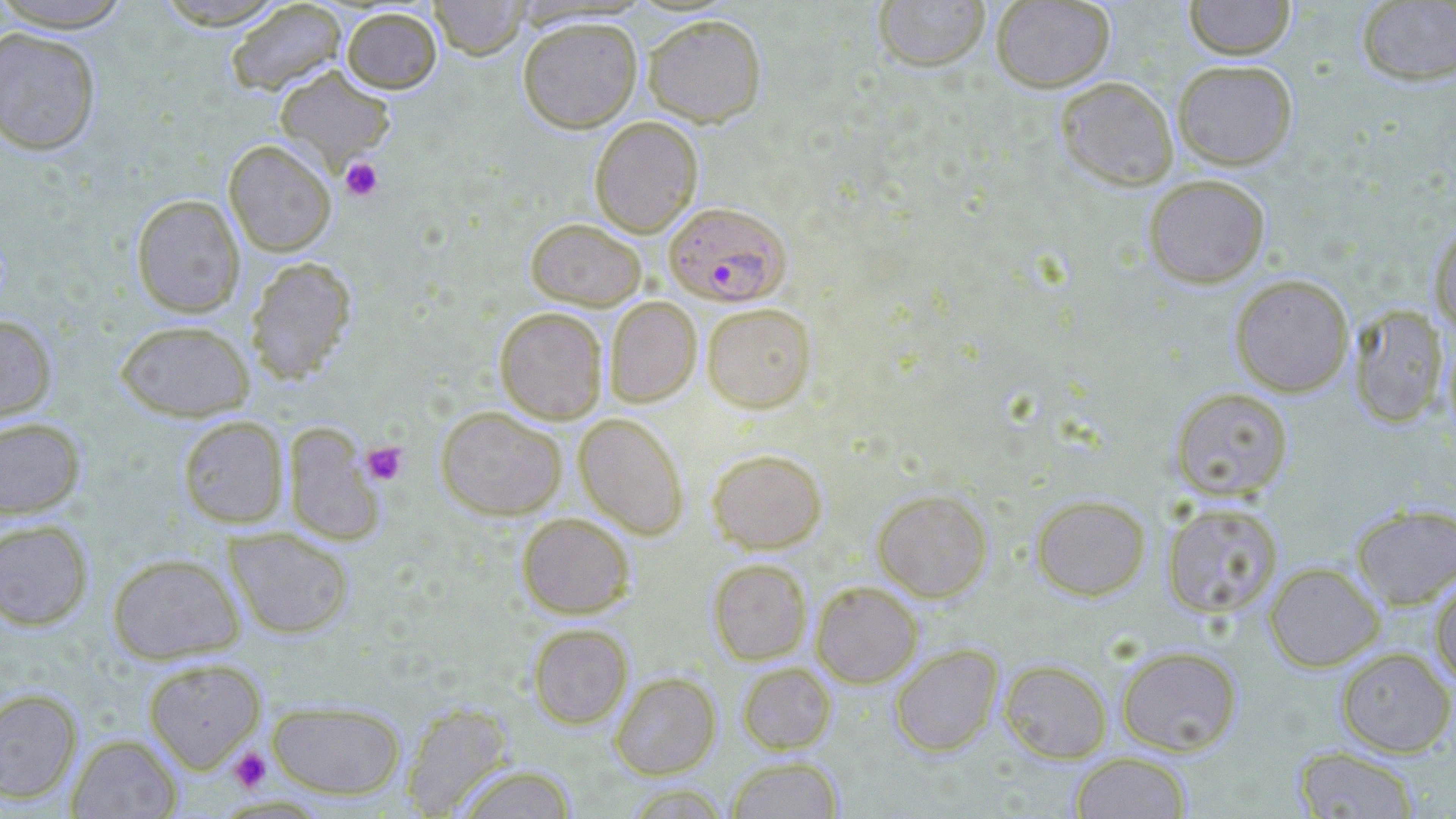

Summary:
  - Coordinate format: approximate bounding boxes as (x1,y1)-(x2,y2) corner pairs in pixels
  - Platelet locations: (340,157)-(383,201), (361,441)-(408,485), (228,747)-(272,792)
  - Uninfected red blood cell locations: (0,0)-(135,32), (150,0)-(290,29), (428,0)-(529,60), (873,0)-(990,72), (991,0)-(1114,92), (1184,0)-(1295,59), (225,1)-(347,97), (1356,1)-(1456,86), (341,6)-(442,93), (642,13)-(767,126), (517,16)-(642,133), (0,27)-(102,155), (1172,60)-(1297,169), (274,65)-(396,170), (1056,76)-(1178,190), (589,116)-(703,237), (223,139)-(337,256), (1143,174)-(1270,288), (131,194)-(245,317), (525,217)-(647,310), (1429,222)-(1456,333), (245,256)-(357,385), (1229,274)-(1354,397), (605,296)-(702,407), (702,303)-(816,412), (1348,304)-(1449,428), (494,306)-(608,424), (0,314)-(57,424), (115,319)-(255,421), (1442,327)-(1456,442), (1170,387)-(1293,501), (435,405)-(567,520), (573,413)-(689,540), (177,415)-(289,528), (0,416)-(85,519), (282,423)-(384,545), (707,448)-(827,553), (872,488)-(992,602), (1031,494)-(1151,600), (1161,502)-(1284,619), (1351,503)-(1456,609), (516,513)-(635,618), (0,518)-(94,631), (224,527)-(354,639), (107,552)-(243,664), (708,559)-(811,665), (1263,562)-(1384,672), (1429,576)-(1456,688), (810,581)-(923,688), (528,623)-(633,728), (890,643)-(1003,757), (1115,645)-(1242,756), (1335,647)-(1456,758), (142,657)-(266,772), (998,659)-(1112,763), (737,662)-(836,754), (610,672)-(721,779), (0,687)-(83,804), (267,700)-(406,799), (400,702)-(516,817), (67,733)-(182,818), (1292,745)-(1421,818), (1069,751)-(1192,818), (726,756)-(844,818), (454,763)-(579,818)
  - Plasmodium falciparum-infected red blood cell locations: (664,201)-(791,307)
  - Slide-level diagnosis: Plasmodium falciparum
  - Preparation: thin blood film
  - Stain: May-Grünwald-Giemsa
  - Modality: light microscopy
  - Field of view: one of a larger specimen
  - Magnification: 1000x
  - Image size: 1456×819 pixels